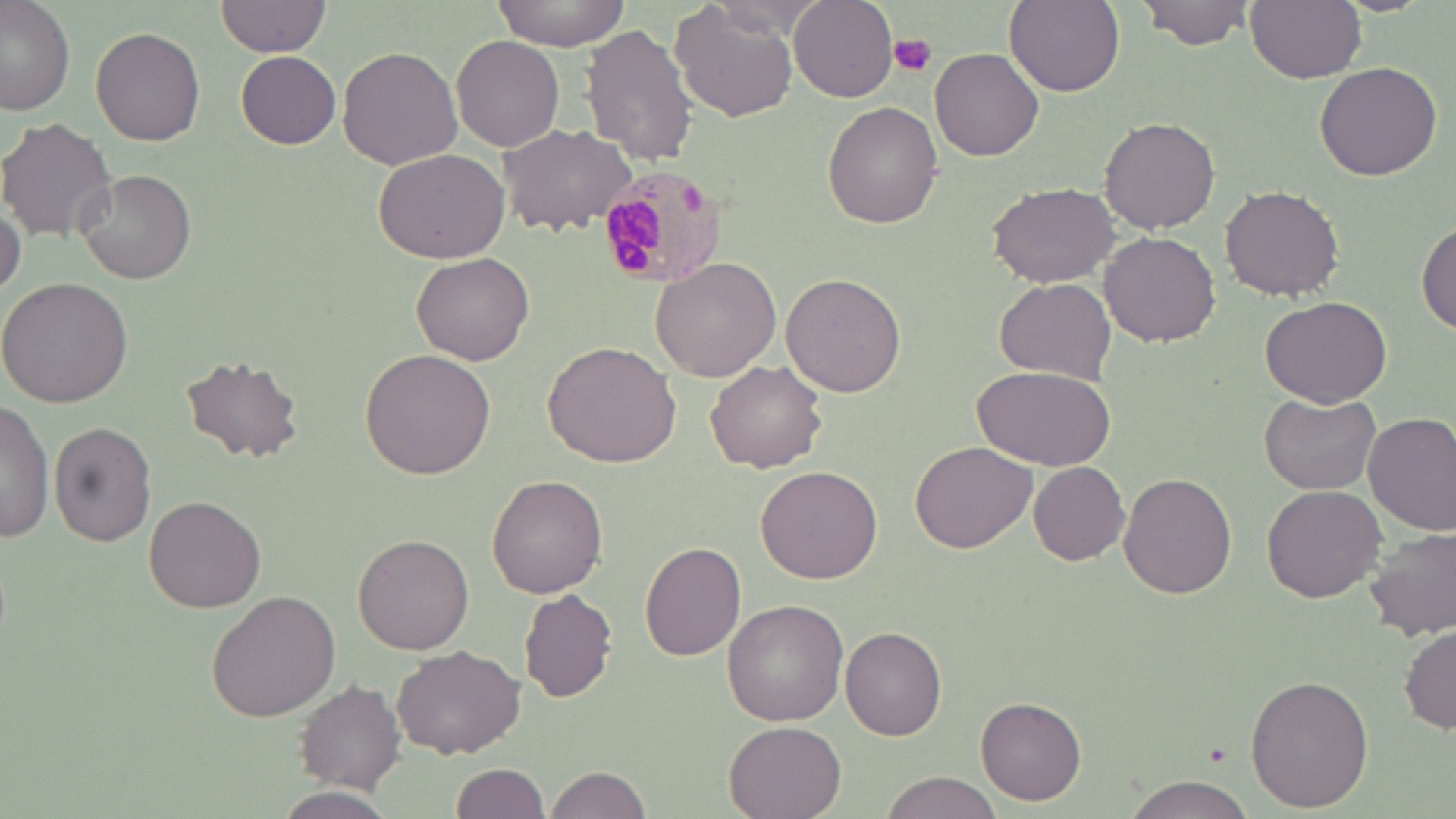

Summary:
  - Coordinate format: approximate bounding boxes as (x1, y1, x2, y2) in pixels
  - Plasmodium malariae-infected red blood cell locations: (593, 165, 731, 291)
  - Platelet locations: (887, 34, 938, 77)
  - Uninfected red blood cell locations: (492, 0, 628, 51), (1004, 0, 1123, 96), (1139, 0, 1254, 50), (1246, 0, 1367, 84), (0, 1, 75, 115), (216, 1, 330, 56), (790, 1, 897, 101), (671, 2, 802, 122), (581, 23, 698, 167), (90, 26, 206, 145), (451, 35, 565, 152), (337, 45, 464, 172), (929, 48, 1045, 163), (236, 51, 340, 148), (1314, 60, 1443, 180), (822, 101, 943, 228), (0, 116, 117, 244), (1099, 116, 1220, 235), (497, 123, 639, 235), (371, 145, 511, 263), (77, 169, 196, 284), (987, 181, 1121, 289), (1221, 184, 1347, 300), (0, 192, 24, 295), (1416, 219, 1456, 334), (1099, 232, 1220, 347), (412, 252, 534, 366), (651, 258, 783, 384), (781, 269, 909, 396), (993, 276, 1115, 385), (0, 277, 133, 408), (1260, 294, 1391, 408), (543, 339, 682, 468), (360, 349, 495, 479), (180, 356, 304, 462), (705, 360, 829, 474), (973, 364, 1114, 468), (1259, 391, 1383, 492), (0, 400, 55, 542), (1363, 411, 1456, 535), (48, 420, 157, 545), (910, 439, 1036, 552), (1029, 463, 1131, 565), (757, 464, 883, 583), (1117, 471, 1238, 600), (488, 473, 609, 598), (1260, 484, 1387, 604), (144, 494, 268, 613), (1365, 525, 1456, 643), (353, 534, 474, 655), (640, 540, 748, 661), (637, 570, 787, 699), (520, 589, 618, 702), (209, 590, 340, 722), (723, 598, 850, 725), (1401, 622, 1456, 736), (841, 627, 947, 740), (392, 645, 525, 758), (1243, 672, 1372, 813), (295, 681, 405, 792), (976, 696, 1086, 804), (724, 720, 848, 819), (451, 764, 551, 818), (543, 764, 650, 819), (877, 772, 1004, 818), (1120, 774, 1261, 818), (275, 787, 398, 818)
  - Slide-level diagnosis: Plasmodium malariae
  - Image size: 1456×819 pixels
  - Preparation: thin blood film
  - Stain: May-Grünwald-Giemsa
  - Field of view: single
  - Modality: optical microscopy
  - Magnification: 1000x